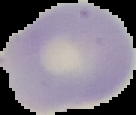
{
  "preparation": "thin blood film",
  "result": "negative for malaria parasites",
  "image_size": "136×115 pixels",
  "image_type": "segmented cell region on a black background"
}